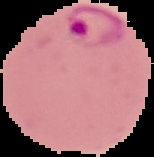
Image is 154×157 pixels. From a thin blood smear. Segmented cell region on a black background. Result: malaria parasites detected.